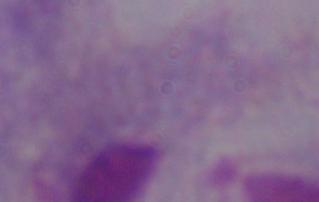

Summary:
  - Modality: micrograph
  - Identification: trichomonad
  - Magnification: 1000x